Classify this cell by malaria status.
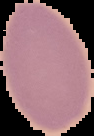
Uninfected.

Summary:
  - Image type: segmented cell region on a black background
  - Preparation: thin blood smear
  - Image size: 94×136 pixels